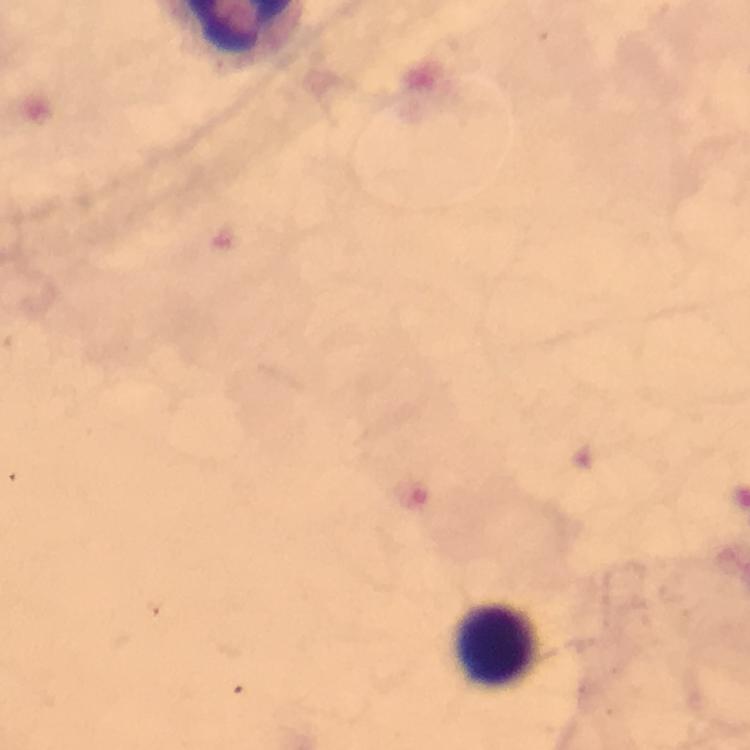

{
  "image_size": "750×750 pixels",
  "preparation": "thick blood film",
  "context": "from a diagnostic examination for malaria",
  "magnification": "100x",
  "leukocyte_locations": "approximate centers as {x, y} in pixels: {495, 646}",
  "malaria_parasites": "none detected",
  "stain": "Giemsa",
  "cropped_from": "one field of view",
  "capture": "smartphone camera through the microscope",
  "immersion_oil": "used"
}